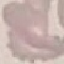

Summary:
  - Result: negative for malaria parasites
  - Preparation: thin blood film
  - Stain: Giemsa
  - Capture: smartphone camera at the microscope eyepiece
  - Image type: automatically extracted cell patch, resized to 64 × 64 pixels